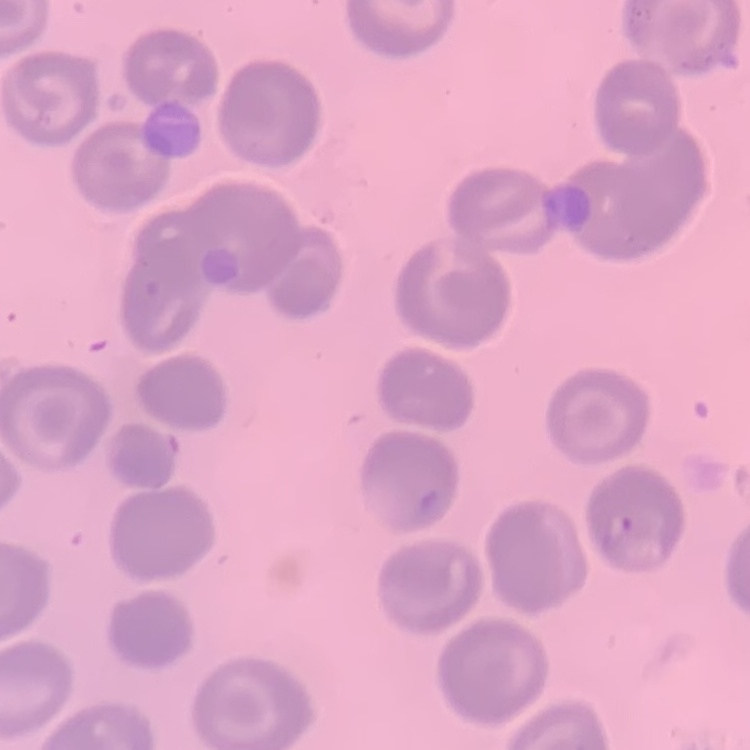
The erythrocytes show no rouleaux formation. Thin blood film. Square crop of a larger photomicrograph. Field's or Giemsa stain.